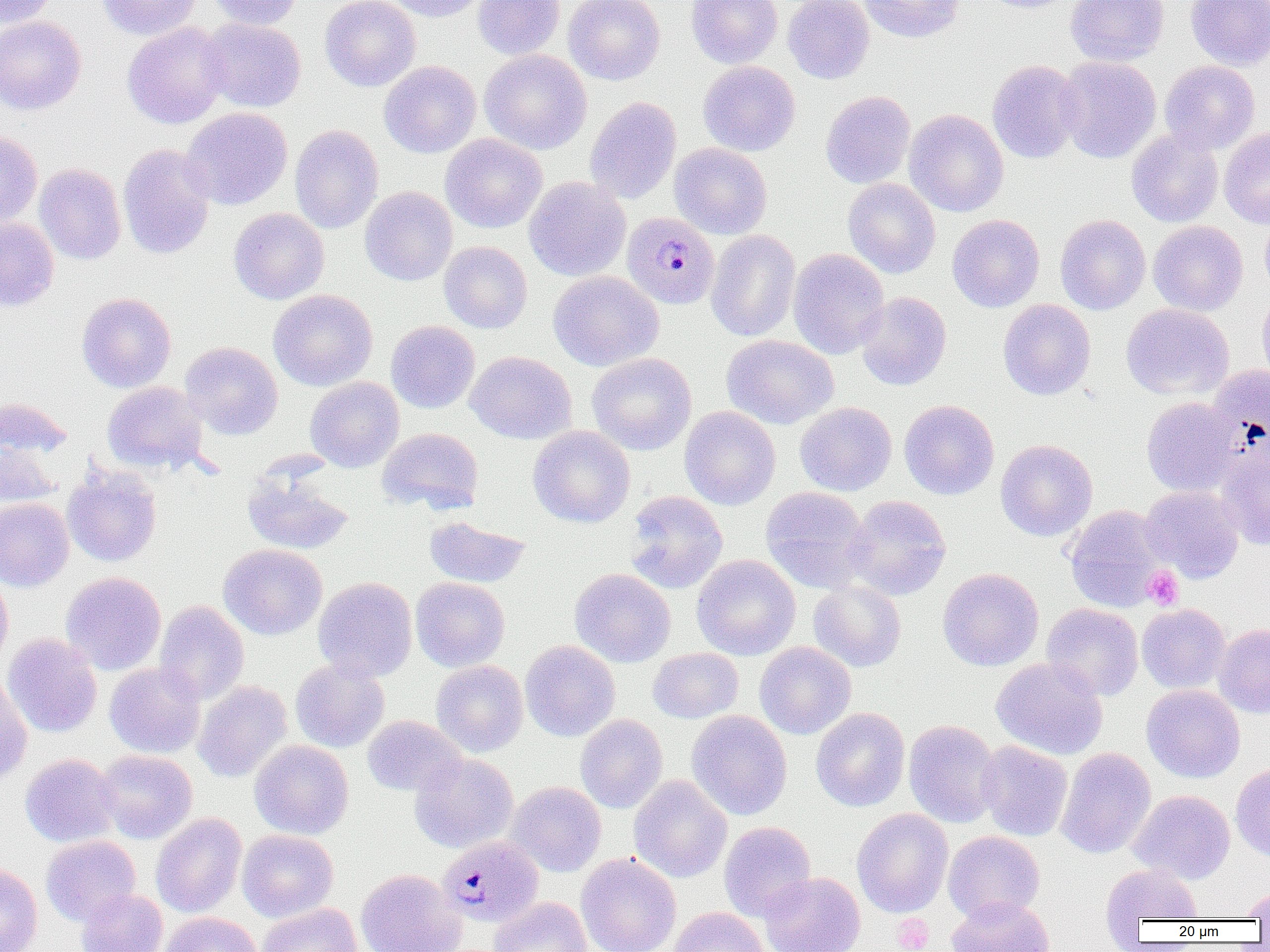

Approximate bounding boxes as (x1, y1, x2, y2) in pixels. Uninfected red blood cell locations: (1, 0, 59, 29), (97, 0, 200, 40), (205, 0, 304, 30), (320, 0, 421, 91), (384, 0, 490, 22), (473, 0, 565, 60), (564, 0, 665, 85), (687, 0, 782, 68), (783, 0, 874, 84), (860, 0, 966, 43), (981, 0, 1082, 13), (1066, 0, 1169, 66), (1185, 0, 1270, 71), (0, 15, 87, 115), (199, 18, 306, 112), (122, 22, 230, 129), (480, 49, 592, 154), (1056, 56, 1161, 163), (379, 60, 481, 158), (698, 60, 801, 156), (986, 60, 1084, 163), (1160, 60, 1260, 154), (820, 90, 915, 188), (584, 96, 681, 204), (181, 107, 293, 211), (904, 109, 1008, 217), (290, 125, 383, 234), (1219, 127, 1270, 229), (1126, 129, 1224, 227), (0, 130, 43, 227), (440, 133, 547, 233), (117, 143, 216, 260), (670, 143, 772, 239), (34, 163, 127, 264), (524, 176, 631, 281), (842, 178, 941, 278), (360, 186, 458, 286), (228, 208, 329, 304), (1259, 212, 1270, 297), (947, 214, 1045, 312), (1055, 214, 1151, 314), (0, 216, 59, 311), (1148, 220, 1248, 316), (705, 229, 801, 342), (439, 241, 532, 333), (788, 248, 889, 360), (548, 270, 664, 371), (268, 289, 377, 391), (1257, 290, 1270, 387), (76, 292, 176, 393), (856, 292, 952, 390), (998, 299, 1096, 400), (1121, 303, 1234, 400), (386, 321, 480, 413), (722, 334, 838, 429), (180, 341, 283, 440), (466, 351, 577, 444), (587, 352, 697, 455), (1207, 365, 1270, 461), (305, 376, 404, 472), (102, 381, 208, 474), (0, 397, 74, 459), (1141, 397, 1243, 496), (899, 399, 999, 500), (795, 402, 897, 496), (679, 406, 780, 510), (528, 425, 635, 528), (376, 427, 483, 514), (0, 437, 64, 507), (995, 439, 1098, 541), (1215, 443, 1270, 550), (62, 463, 163, 567), (241, 465, 354, 555), (1140, 485, 1245, 582), (760, 486, 872, 593), (624, 490, 728, 594), (844, 495, 951, 600), (0, 498, 73, 592), (1065, 505, 1168, 611), (424, 516, 531, 588), (218, 544, 328, 640), (691, 554, 801, 660), (937, 567, 1044, 671), (569, 568, 676, 667), (0, 570, 13, 670), (60, 571, 166, 675), (313, 577, 417, 681), (410, 577, 510, 672), (808, 581, 906, 672), (154, 601, 249, 704), (1042, 603, 1144, 701), (1137, 603, 1231, 693), (1213, 623, 1270, 719), (2, 633, 103, 738), (520, 640, 620, 742), (754, 641, 856, 739), (647, 648, 743, 723), (991, 657, 1108, 760), (290, 658, 390, 753), (431, 660, 528, 756), (104, 662, 206, 759), (0, 673, 32, 786), (193, 680, 293, 782), (1141, 684, 1245, 783), (811, 707, 910, 812), (686, 710, 792, 820), (575, 714, 667, 813), (362, 715, 466, 796), (903, 719, 1002, 827), (249, 739, 353, 839), (977, 740, 1073, 841), (1055, 747, 1156, 859), (94, 749, 197, 844), (20, 753, 121, 847), (409, 753, 518, 853), (1230, 764, 1270, 862), (628, 775, 732, 883), (506, 782, 607, 877), (1128, 790, 1235, 884), (851, 808, 953, 918), (151, 813, 247, 918), (718, 821, 816, 921), (237, 829, 339, 922), (942, 831, 1045, 923), (40, 835, 141, 926), (576, 853, 681, 952), (0, 863, 43, 952), (1101, 864, 1203, 928), (356, 868, 466, 952), (759, 872, 865, 952), (1241, 887, 1270, 920), (76, 889, 168, 952), (946, 895, 1055, 952), (489, 896, 592, 952), (257, 902, 362, 952), (666, 906, 770, 952), (156, 912, 262, 952). Plasmodium malariae-infected red blood cell locations: (622, 212, 720, 309), (437, 836, 544, 927). Platelet locations: (1142, 566, 1183, 609), (893, 914, 934, 951). Slide-level diagnosis: Plasmodium malariae. Thin blood film. Image is 1270×952 pixels. One field of a larger specimen. Light microscopy. 1000x magnification.